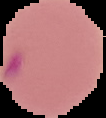

Summary:
  - Image size: 106×118 pixels
  - Image type: cell region segmented out of the field of view; surrounding area masked to black
  - Result: malaria parasites identified
  - Preparation: thin blood smear